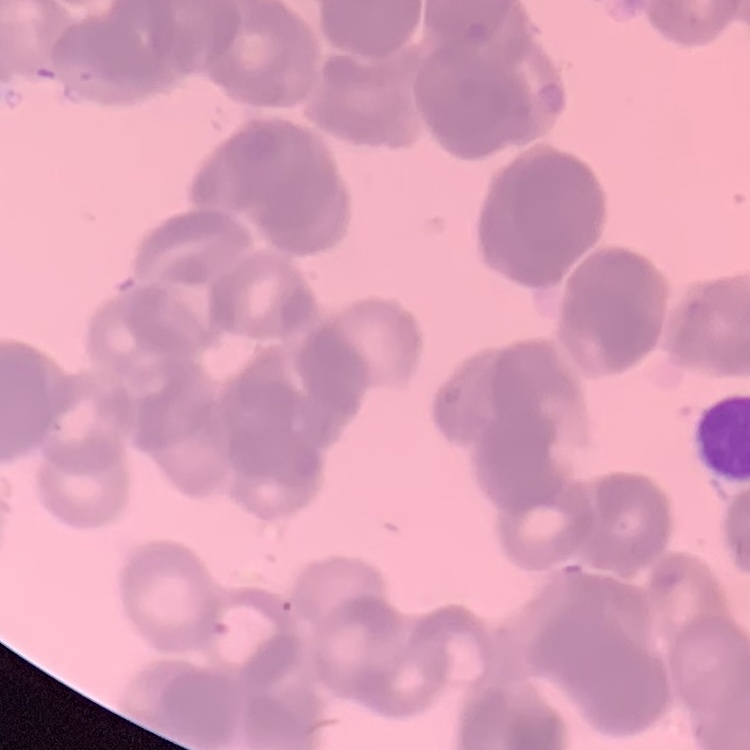

The erythrocytes exhibit rouleaux formation. Stained with either Field's or Giemsa. Square crop of a larger photomicrograph. Thin peripheral smear.